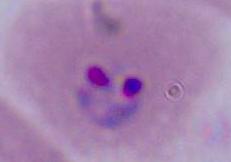

magnification = 400x or 1000x
modality = photomicrograph
identification = Plasmodium